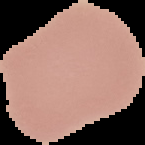
malaria_status: uninfected
preparation: thin blood smear
image_size: 145×145 pixels
image_type: segmented cell region with the area outside set to black